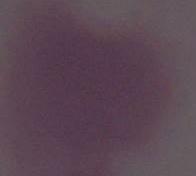

Summary:
  - Magnification: 1000x
  - Identification: erythrocyte
  - Modality: photomicrograph